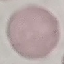
Summary:
  - Result: no malaria parasites seen
  - Preparation: thin blood film
  - Stain: Giemsa
  - Image type: cell patch, automatically extracted from a larger field of view and resized to 64 × 64 pixels
  - Capture: smartphone through the microscope eyepiece